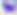
Summary:
  - Modality: photomicrograph
  - Magnification: 400x
  - Identification: Toxoplasma gondii